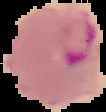

Image is 106×112 pixels. From a thin blood smear. Malaria status: parasitized. The area outside the segmented cell region is set to black.